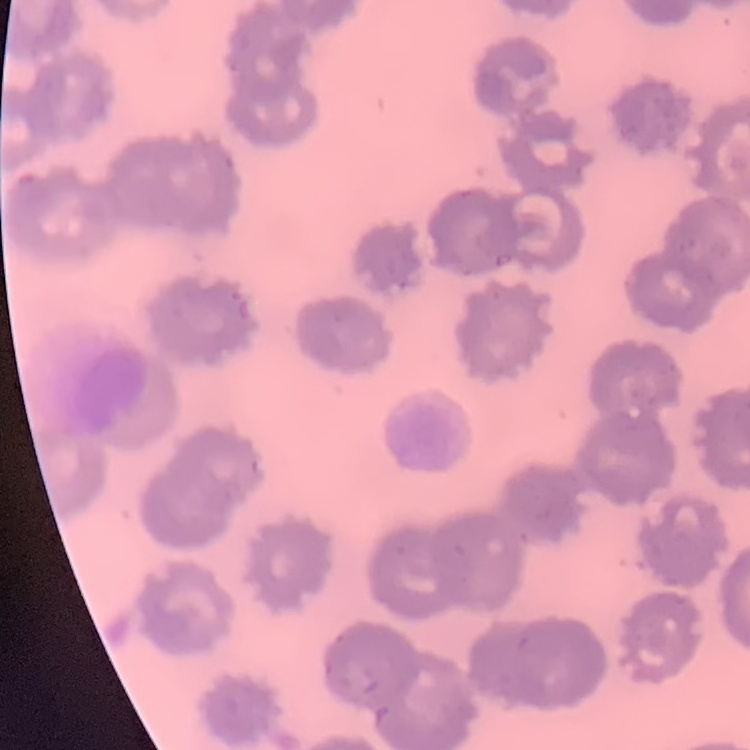
The erythrocytes show no rouleaux formation. Square crop of a larger photomicrograph. Field's or Giemsa stain. Thin peripheral smear.